Report the malaria status of this cell.
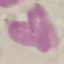
It is uninfected.

capture: smartphone through the microscope eyepiece
preparation: thin smear
stain: Giemsa
image_type: cell patch, automatically extracted from a larger field of view and resized to 64 × 64 pixels